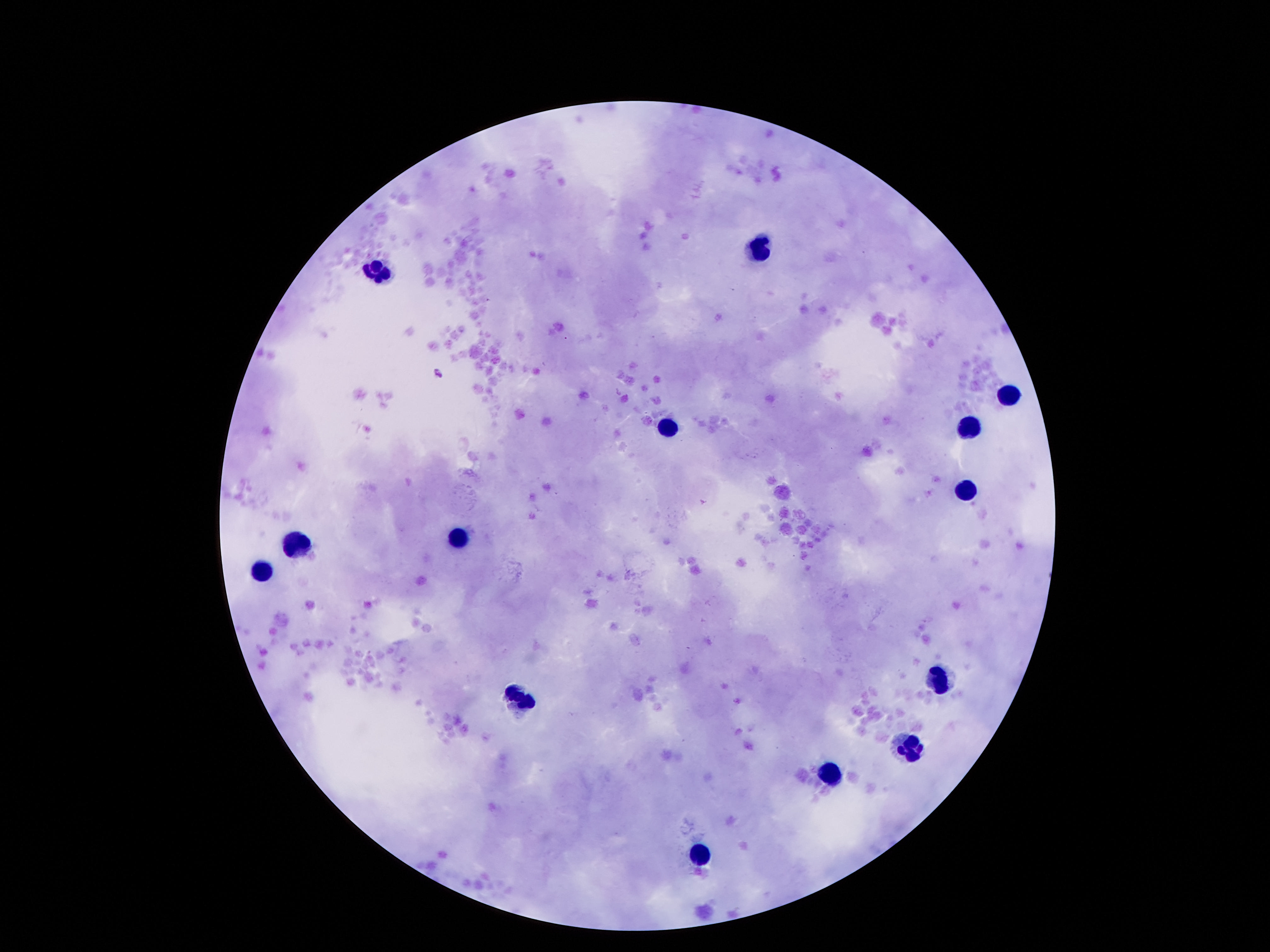

magnification = 100x
patient malaria status = not infected
field of view = single
capture = smartphone camera through the microscope eyepiece
leukocyte locations = approximate centers as {x, y} in pixels: {759, 248}, {377, 271}, {1009, 397}, {669, 426}, {969, 428}, {965, 495}, {457, 533}, {297, 542}, {260, 573}, {940, 678}, {522, 701}, {911, 747}, {833, 772}, {701, 852}
image size = 1270×952 pixels
preparation = thick blood film
stain = Giemsa